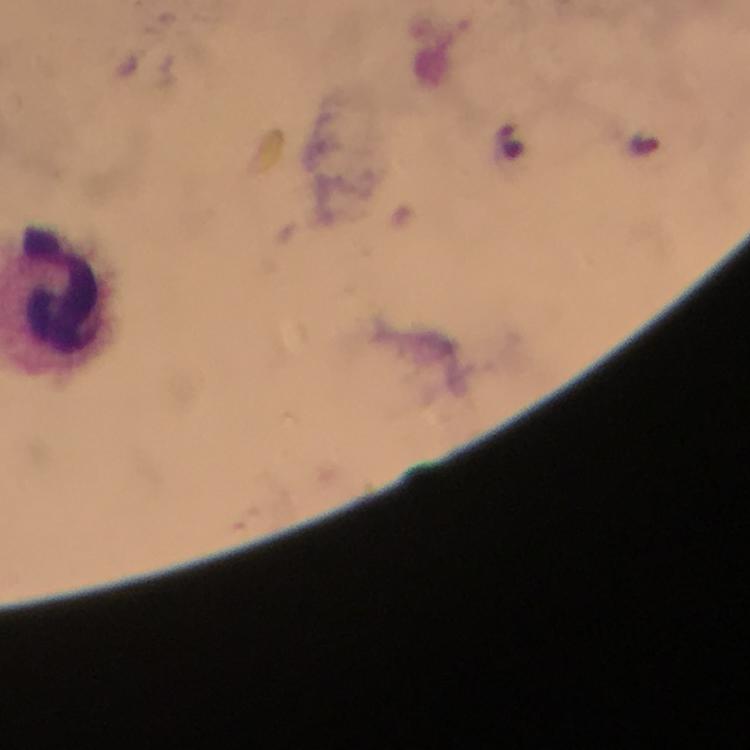
{
  "capture": "smartphone photograph through a microscope",
  "stain": "Giemsa",
  "plasmodium_parasite_locations": "approximate centers as {x, y} in pixels: {512, 140}, {643, 145}",
  "magnification": "100x",
  "preparation": "thick blood film",
  "cropped_from": "one field of view",
  "leukocyte_locations": "approximate centers as {x, y} in pixels: {53, 285}",
  "immersion_oil": "applied",
  "image_size": "750×750 pixels",
  "context": "from a malaria diagnostic workup"
}